Give a bounding box for every malaria parasite.
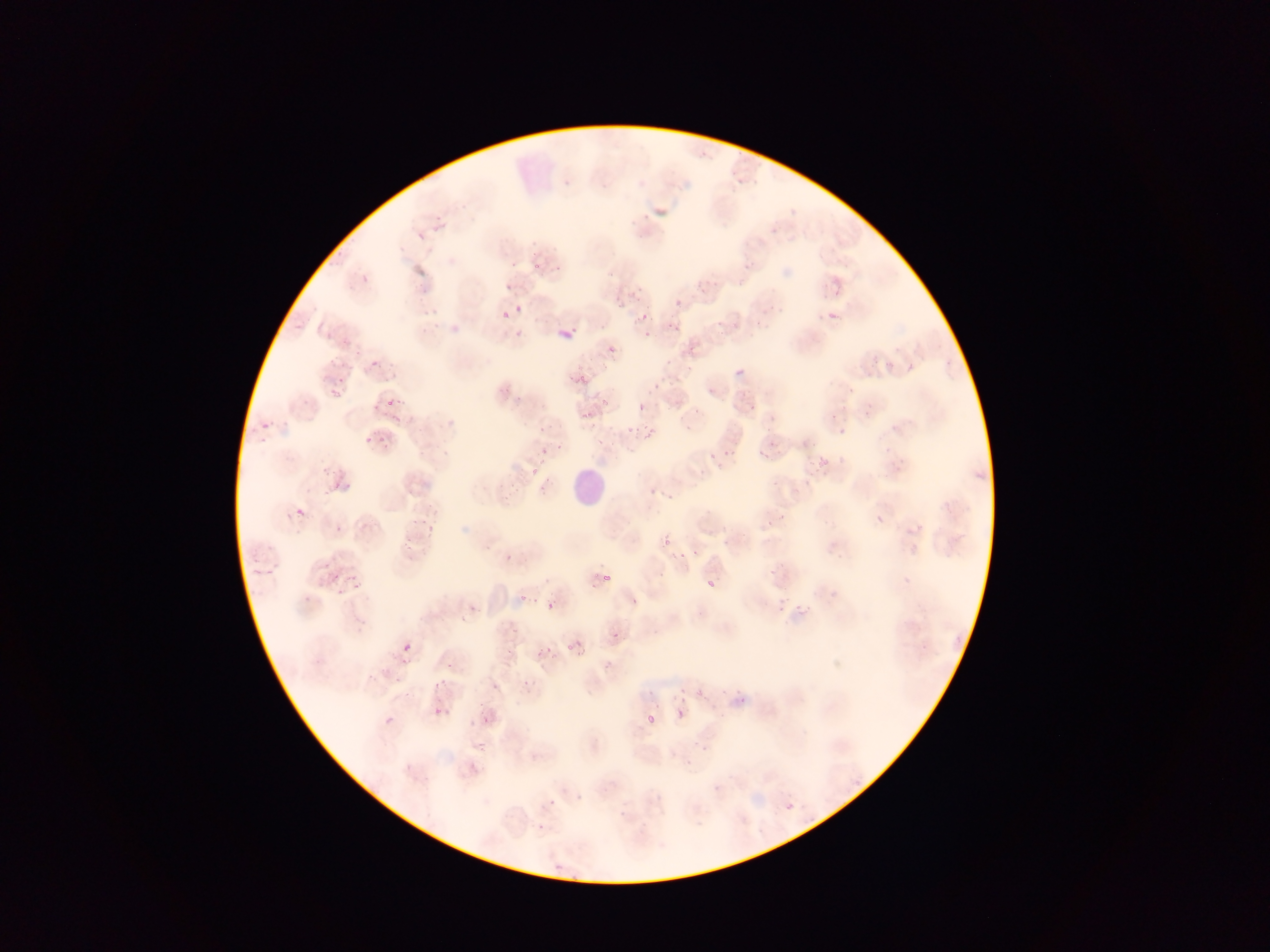

Approximate bounding boxes as (left, top, right, bottom) in pixels.
Malaria parasites: (532, 263, 540, 269), (736, 276, 747, 288), (836, 284, 842, 296), (503, 310, 506, 322), (829, 312, 838, 320), (640, 315, 648, 320), (556, 323, 575, 340), (676, 326, 680, 334), (608, 346, 616, 353), (371, 360, 380, 367), (905, 364, 914, 371), (737, 366, 745, 375), (579, 374, 590, 382), (580, 382, 589, 387), (331, 390, 344, 399), (387, 396, 396, 405), (600, 398, 607, 406), (638, 403, 643, 414), (262, 422, 269, 430), (642, 424, 650, 431), (840, 425, 845, 438), (624, 426, 633, 433), (650, 427, 658, 436), (378, 435, 384, 444), (363, 437, 370, 445), (541, 447, 548, 455), (759, 448, 768, 462), (709, 453, 717, 461), (820, 455, 828, 466), (294, 507, 307, 519), (877, 512, 887, 523), (663, 540, 671, 545), (507, 553, 515, 561), (679, 554, 688, 560), (334, 573, 342, 581), (603, 574, 610, 583), (343, 575, 350, 583), (705, 580, 716, 588), (353, 582, 362, 590), (335, 586, 346, 598), (518, 595, 528, 605), (545, 601, 556, 611), (777, 604, 785, 612), (800, 610, 806, 619), (611, 630, 622, 639), (575, 639, 583, 647), (403, 643, 410, 651), (545, 646, 553, 652), (565, 646, 573, 652), (537, 648, 542, 658), (394, 675, 399, 683), (679, 686, 687, 692), (671, 694, 679, 702), (680, 697, 688, 703), (677, 708, 683, 719), (434, 709, 442, 715), (647, 711, 658, 725), (484, 715, 488, 724), (386, 717, 395, 724), (477, 741, 485, 746), (407, 759, 412, 771) | approximate (x, y) pixel centers of objects too small to bound: (557, 267), (518, 309), (669, 324), (647, 335), (656, 384), (601, 413), (337, 485), (432, 529), (695, 552), (635, 601), (404, 662), (442, 682), (437, 686), (698, 693).

Summary:
  - Leukocyte locations: (570, 470, 607, 509)
  - Country: Ghana
  - Field of view: single
  - Image size: 1270×952 pixels
  - Preparation: thin blood film
  - Capture: mobile-phone photograph through a microscope